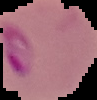

Summary:
  - Image size: 97×100 pixels
  - Preparation: thin blood smear
  - Malaria status: parasitized
  - Image type: segmented cell region on a black background